Give the position of every Plasmodium parasite.
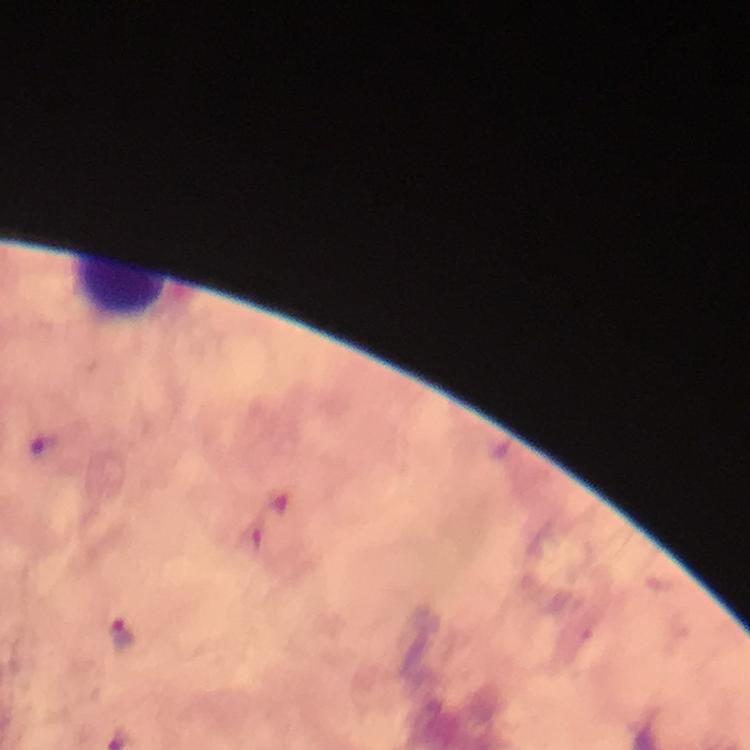

Approximate centers as {x, y} in pixels.
Plasmodium parasites: {121, 632}.

From a malaria diagnostic workup. Immersion oil was used. Giemsa-stained preparation. 100x magnification. Cropped region of a single field of view. Photographed through the microscope with a smartphone camera. Image is 750×750 pixels. Thick smear.